Assess this cell for malaria.
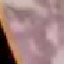

It is uninfected.

Photographed with a smartphone camera at the microscope eyepiece. Thin blood film. Cell patch, automatically extracted from a larger field of view and resized to 64 × 64 pixels. Giemsa stain.